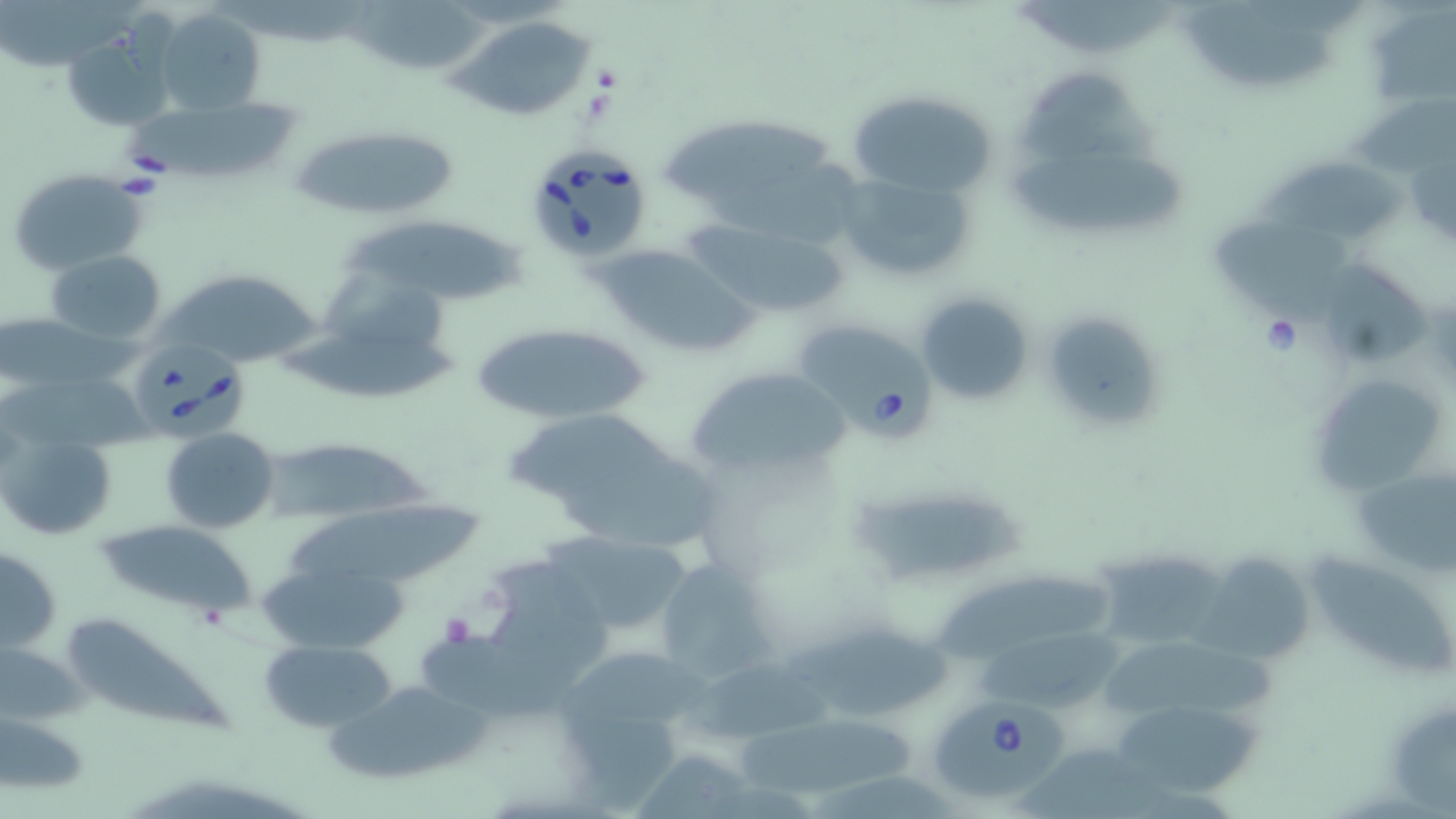
slide-level diagnosis = Babesia divergens
uninfected red blood cell locations = approximate bounding boxes as named x1/y1/x2/y2 corners in pixels: (x1=346, y1=2, x2=495, y2=70), (x1=152, y1=9, x2=264, y2=116), (x1=1189, y1=13, x2=1337, y2=87), (x1=1369, y1=13, x2=1456, y2=99), (x1=453, y1=15, x2=597, y2=121), (x1=61, y1=31, x2=176, y2=134), (x1=1015, y1=70, x2=1170, y2=162), (x1=846, y1=87, x2=998, y2=201), (x1=117, y1=96, x2=316, y2=173), (x1=660, y1=108, x2=833, y2=202), (x1=288, y1=126, x2=459, y2=219), (x1=1009, y1=150, x2=1193, y2=237), (x1=1251, y1=155, x2=1414, y2=239), (x1=832, y1=166, x2=980, y2=288), (x1=5, y1=168, x2=150, y2=275), (x1=682, y1=215, x2=852, y2=318), (x1=339, y1=216, x2=534, y2=296), (x1=1212, y1=220, x2=1354, y2=324), (x1=592, y1=242, x2=761, y2=363), (x1=46, y1=250, x2=167, y2=345), (x1=1323, y1=264, x2=1433, y2=367), (x1=151, y1=265, x2=334, y2=365), (x1=314, y1=268, x2=458, y2=354), (x1=914, y1=291, x2=1036, y2=408), (x1=0, y1=308, x2=150, y2=390), (x1=1042, y1=318, x2=1161, y2=422), (x1=273, y1=320, x2=462, y2=399), (x1=468, y1=322, x2=655, y2=424), (x1=682, y1=362, x2=856, y2=481), (x1=0, y1=369, x2=151, y2=449), (x1=1322, y1=383, x2=1444, y2=497), (x1=505, y1=408, x2=722, y2=548), (x1=160, y1=427, x2=280, y2=533), (x1=4, y1=431, x2=118, y2=542), (x1=260, y1=441, x2=444, y2=515), (x1=841, y1=480, x2=1034, y2=582), (x1=287, y1=503, x2=493, y2=586), (x1=90, y1=519, x2=255, y2=621), (x1=538, y1=528, x2=699, y2=642), (x1=1, y1=545, x2=62, y2=655), (x1=1186, y1=549, x2=1321, y2=672), (x1=1306, y1=550, x2=1451, y2=674), (x1=262, y1=556, x2=412, y2=654), (x1=655, y1=558, x2=779, y2=683), (x1=1098, y1=558, x2=1240, y2=645), (x1=933, y1=570, x2=1115, y2=658), (x1=67, y1=615, x2=232, y2=735), (x1=778, y1=622, x2=953, y2=721), (x1=260, y1=637, x2=397, y2=732), (x1=976, y1=637, x2=1127, y2=711), (x1=0, y1=640, x2=87, y2=728), (x1=558, y1=642, x2=725, y2=733), (x1=1107, y1=645, x2=1288, y2=716), (x1=673, y1=663, x2=843, y2=745), (x1=327, y1=680, x2=500, y2=782), (x1=1388, y1=702, x2=1456, y2=819), (x1=1114, y1=704, x2=1271, y2=796), (x1=0, y1=709, x2=90, y2=797), (x1=740, y1=721, x2=918, y2=799), (x1=633, y1=749, x2=806, y2=819), (x1=1022, y1=752, x2=1172, y2=819)
image size = 1456×819 pixels
magnification = 1000x
Babesia divergens-infected red blood cell locations = approximate bounding boxes as named x1/y1/x2/y2 corners in pixels: (x1=524, y1=146, x2=653, y2=265), (x1=793, y1=319, x2=936, y2=443), (x1=129, y1=339, x2=248, y2=439), (x1=933, y1=694, x2=1064, y2=803)
modality = light microscopy
platelet locations = approximate bounding boxes as named x1/y1/x2/y2 corners in pixels: (x1=440, y1=612, x2=474, y2=646)
stain = May-Grünwald-Giemsa
field of view = one of a larger specimen
preparation = thin blood smear